Identify the cell.
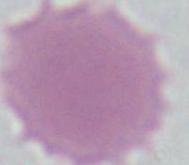
An erythrocyte.

Photomicrograph. 1000x magnification.